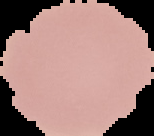

preparation = thin blood film
image type = cell region segmented out of the field of view; surrounding area masked to black
image size = 154×136 pixels
malaria status = uninfected